Outline each blood parasite and name the species.
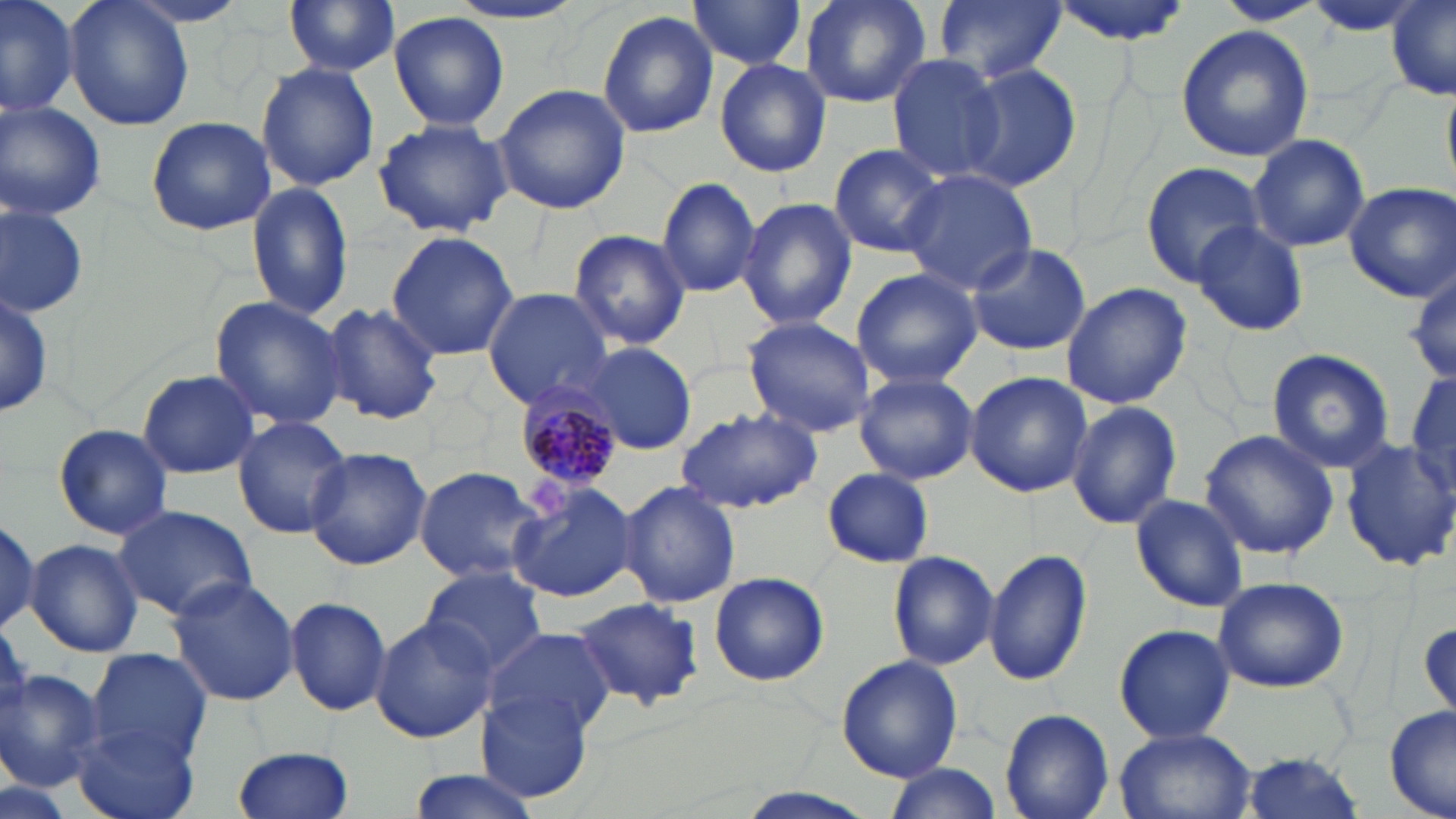
Approximate bounding boxes as named x1/y1/x2/y2 corners in pixels.
Plasmodium malariae-infected red blood cells: (x1=507, y1=384, x2=620, y2=493).
No Plasmodium falciparum, Plasmodium ovale, Plasmodium vivax, Babesia divergens, or Trypanosoma brucei observed.

Uninfected red blood cell locations: (x1=0, y1=0, x2=78, y2=120), (x1=63, y1=0, x2=195, y2=133), (x1=282, y1=0, x2=402, y2=76), (x1=437, y1=0, x2=591, y2=29), (x1=801, y1=0, x2=931, y2=109), (x1=932, y1=0, x2=1065, y2=85), (x1=1047, y1=0, x2=1191, y2=45), (x1=1214, y1=0, x2=1326, y2=25), (x1=1302, y1=1, x2=1431, y2=38), (x1=1387, y1=1, x2=1456, y2=101), (x1=687, y1=2, x2=809, y2=72), (x1=389, y1=11, x2=511, y2=132), (x1=597, y1=11, x2=720, y2=139), (x1=1175, y1=25, x2=1313, y2=162), (x1=886, y1=54, x2=1005, y2=181), (x1=714, y1=59, x2=830, y2=177), (x1=256, y1=62, x2=379, y2=191), (x1=958, y1=63, x2=1079, y2=191), (x1=493, y1=84, x2=630, y2=215), (x1=0, y1=101, x2=106, y2=221), (x1=146, y1=114, x2=277, y2=236), (x1=372, y1=118, x2=514, y2=238), (x1=1246, y1=134, x2=1371, y2=252), (x1=829, y1=143, x2=951, y2=258), (x1=1139, y1=161, x2=1265, y2=287), (x1=902, y1=169, x2=1037, y2=293), (x1=656, y1=176, x2=762, y2=298), (x1=245, y1=179, x2=359, y2=322), (x1=1345, y1=182, x2=1455, y2=301), (x1=736, y1=196, x2=857, y2=330), (x1=0, y1=203, x2=89, y2=317), (x1=1191, y1=221, x2=1308, y2=337), (x1=572, y1=229, x2=690, y2=349), (x1=385, y1=231, x2=519, y2=361), (x1=964, y1=244, x2=1092, y2=356), (x1=849, y1=267, x2=982, y2=389), (x1=1060, y1=281, x2=1192, y2=408), (x1=0, y1=283, x2=53, y2=423), (x1=481, y1=288, x2=615, y2=410), (x1=209, y1=295, x2=348, y2=431), (x1=321, y1=302, x2=445, y2=426), (x1=740, y1=316, x2=878, y2=437), (x1=581, y1=340, x2=700, y2=455), (x1=1267, y1=349, x2=1395, y2=471), (x1=1409, y1=366, x2=1456, y2=500), (x1=137, y1=368, x2=262, y2=479), (x1=853, y1=372, x2=978, y2=485), (x1=965, y1=372, x2=1093, y2=498), (x1=1066, y1=400, x2=1181, y2=530), (x1=676, y1=409, x2=823, y2=514), (x1=232, y1=415, x2=352, y2=540), (x1=53, y1=423, x2=176, y2=540), (x1=1200, y1=428, x2=1339, y2=560), (x1=1340, y1=437, x2=1456, y2=572), (x1=306, y1=448, x2=433, y2=571), (x1=413, y1=465, x2=548, y2=585), (x1=822, y1=467, x2=935, y2=567), (x1=505, y1=478, x2=637, y2=604), (x1=618, y1=480, x2=741, y2=610), (x1=1132, y1=494, x2=1249, y2=612), (x1=113, y1=504, x2=259, y2=624), (x1=0, y1=511, x2=46, y2=638), (x1=25, y1=538, x2=144, y2=658), (x1=985, y1=548, x2=1090, y2=687), (x1=887, y1=551, x2=999, y2=670), (x1=419, y1=565, x2=548, y2=676), (x1=166, y1=574, x2=301, y2=706), (x1=706, y1=574, x2=832, y2=688), (x1=1210, y1=576, x2=1350, y2=693), (x1=285, y1=595, x2=392, y2=717), (x1=574, y1=597, x2=704, y2=710), (x1=370, y1=616, x2=496, y2=743), (x1=1418, y1=617, x2=1455, y2=724), (x1=1113, y1=624, x2=1235, y2=746), (x1=480, y1=626, x2=618, y2=738), (x1=86, y1=648, x2=214, y2=761), (x1=836, y1=655, x2=963, y2=781), (x1=0, y1=668, x2=106, y2=790), (x1=478, y1=690, x2=590, y2=802), (x1=1385, y1=706, x2=1455, y2=819), (x1=999, y1=707, x2=1114, y2=819), (x1=73, y1=721, x2=201, y2=819), (x1=1114, y1=728, x2=1259, y2=819), (x1=231, y1=745, x2=355, y2=819), (x1=1236, y1=752, x2=1366, y2=819), (x1=880, y1=764, x2=1000, y2=819), (x1=404, y1=769, x2=548, y2=819), (x1=726, y1=789, x2=885, y2=819). Slide-level diagnosis: Plasmodium malariae. May-Grünwald-Giemsa stain. Light microscopy. Thin blood film. Image is 1456×819 pixels. Single field of view. 1000x magnification.